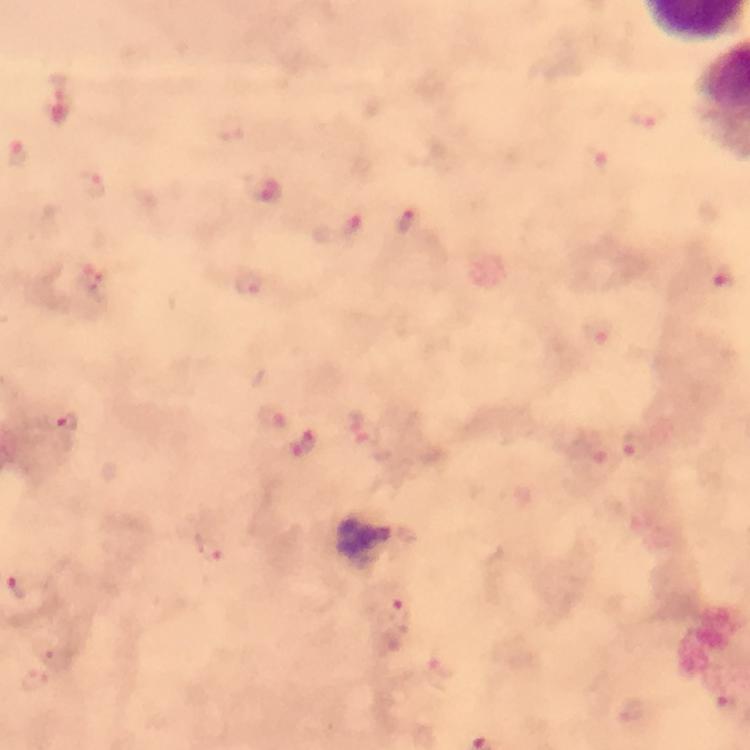

Approximate object centers, in pixels from the top-left corner.
Summary:
  - Plasmodium parasite locations: (x=61, y=97), (x=649, y=115), (x=599, y=162), (x=94, y=188), (x=263, y=190), (x=408, y=222), (x=351, y=228), (x=724, y=279), (x=249, y=285), (x=597, y=333), (x=270, y=416), (x=65, y=423), (x=305, y=445), (x=633, y=447), (x=594, y=452), (x=212, y=546), (x=18, y=585), (x=395, y=603), (x=446, y=658), (x=34, y=681)
  - Context: from a malaria diagnostic workup
  - Immersion oil: applied
  - Preparation: thick blood smear
  - Image size: 750×750 pixels
  - Magnification: 100x
  - Cropped from: one field of view
  - Capture: smartphone camera through the microscope
  - Stain: Giemsa